Point out each Plasmodium parasite.
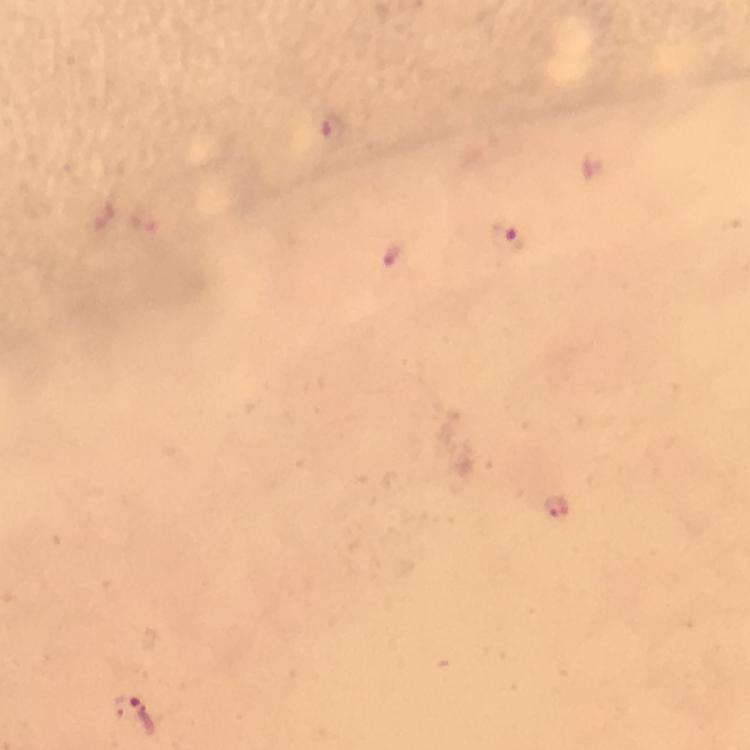

Approximate centers as (x, y) in pixels.
Plasmodium parasites: (331, 128), (509, 239), (395, 255), (558, 504), (132, 711).

stain: Giemsa
immersion_oil: used
capture: smartphone photograph through a microscope
context: from a diagnostic examination for malaria
cropped_from: one field of view
preparation: thick blood film
image_size: 750×750 pixels
magnification: 100x